State which parasite is depicted.
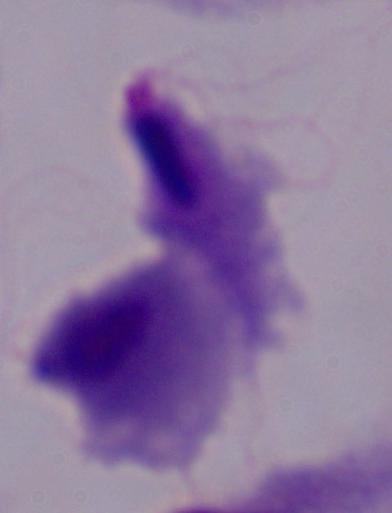

This is a trichomonad.

Summary:
  - Modality: micrograph
  - Magnification: 1000x